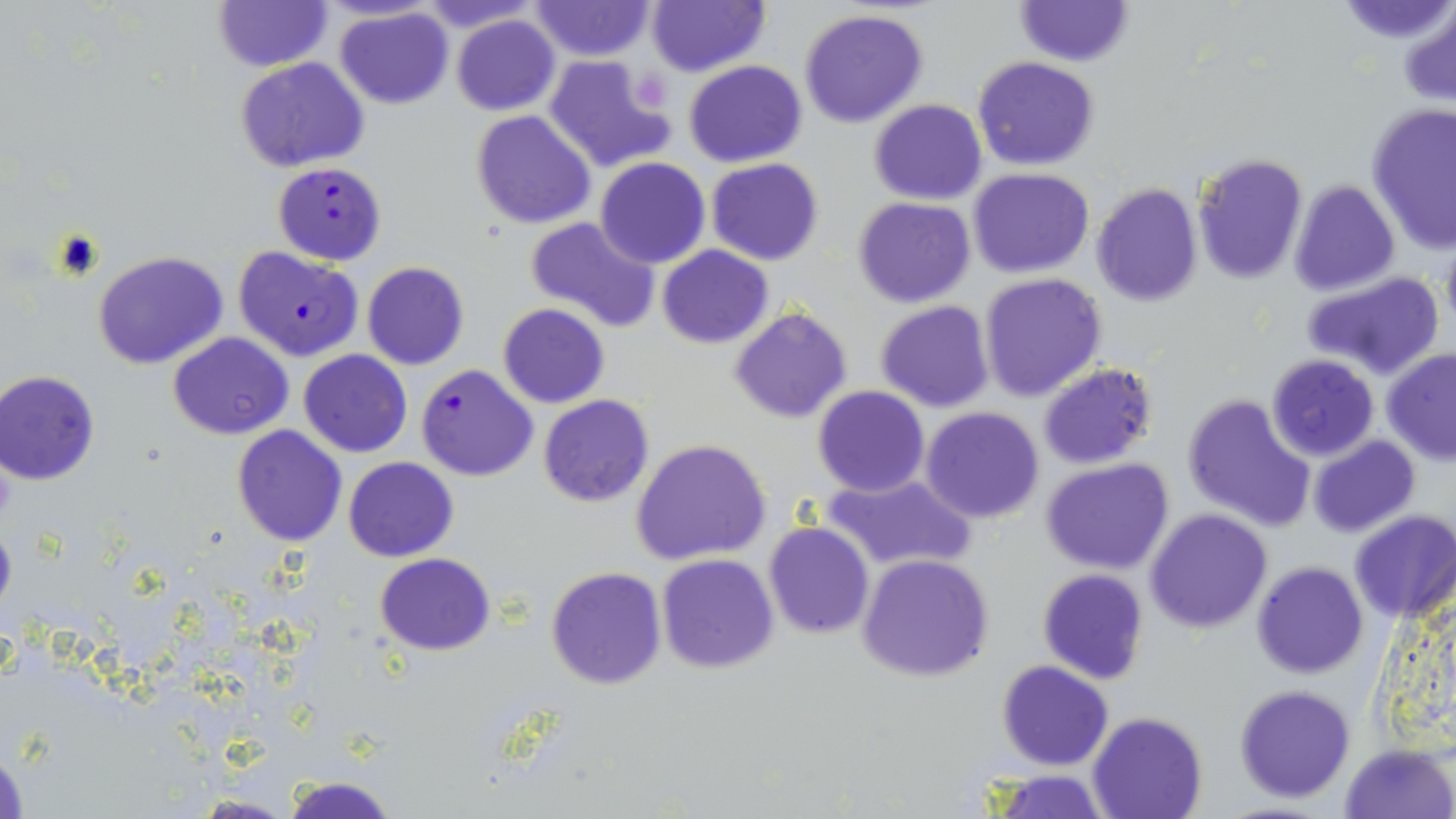

Approximate bounding boxes as (x1,y1)-(x2,y2) corner pairs in pixels. Uninfected red blood cell locations: (213,0)-(330,72), (416,0)-(540,31), (646,0)-(767,76), (1013,0)-(1132,67), (1337,0)-(1456,47), (528,1)-(655,62), (1400,3)-(1456,109), (335,7)-(454,110), (798,9)-(930,128), (452,13)-(561,116), (544,52)-(675,173), (234,57)-(370,172), (973,57)-(1099,171), (683,60)-(807,167), (868,98)-(988,203), (1366,102)-(1456,255), (470,110)-(596,229), (1192,151)-(1308,284), (595,157)-(711,269), (706,157)-(823,266), (968,168)-(1094,277), (1288,180)-(1399,296), (1091,182)-(1202,307), (852,196)-(976,309), (523,215)-(660,333), (1441,230)-(1456,342), (658,245)-(772,348), (94,251)-(228,370), (362,263)-(470,370), (978,272)-(1108,401), (1302,272)-(1444,380), (876,300)-(994,413), (498,303)-(609,408), (728,306)-(852,424), (167,333)-(294,439), (1380,348)-(1456,465), (299,349)-(412,457), (1266,355)-(1383,461), (1037,362)-(1158,469), (1,368)-(101,484), (812,386)-(929,496), (1182,394)-(1315,531), (538,395)-(653,507), (920,407)-(1045,524), (231,425)-(346,546), (1309,435)-(1419,537), (631,439)-(772,567), (344,457)-(457,562), (1040,459)-(1174,574), (820,471)-(976,572), (1145,509)-(1273,632), (1349,510)-(1456,625), (0,520)-(16,620), (763,522)-(876,639), (375,553)-(496,655), (657,554)-(779,674), (857,554)-(993,681), (1251,562)-(1367,679), (545,566)-(667,690), (1036,568)-(1149,684), (995,660)-(1115,770), (1234,685)-(1355,802), (1088,713)-(1208,819), (1341,742)-(1454,818), (1,743)-(29,819), (986,770)-(1111,818), (281,773)-(398,819), (183,794)-(301,818). Platelet locations: (630,70)-(670,109). Plasmodium falciparum-infected red blood cell locations: (272,161)-(386,265), (233,246)-(364,363), (416,363)-(539,482). Slide-level diagnosis: Plasmodium falciparum. Image is 1456×819 pixels. One field of a larger specimen. Light microscopy. 1000x magnification. Thin blood smear. May-Grünwald-Giemsa stain.